Locate every blood parasite and identify its species.
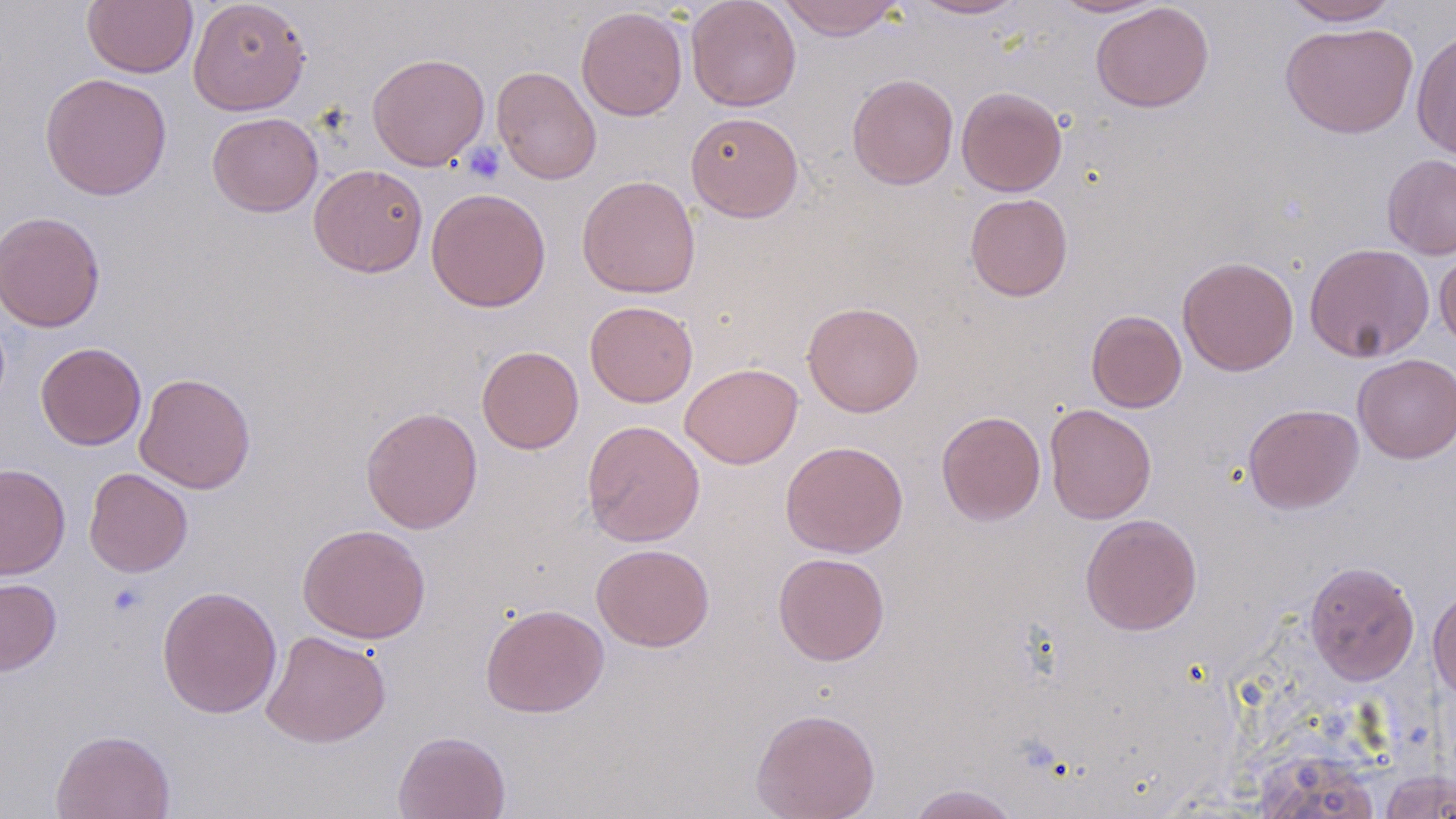
No blood parasites observed.

slide-level diagnosis = no evidence of blood parasites
uninfected red blood cell locations = approximate bounding boxes as [x1, y1, x2, y2] in pixels: [82, 0, 198, 78], [187, 0, 311, 115], [686, 0, 802, 111], [777, 0, 905, 40], [910, 0, 1027, 20], [1054, 0, 1164, 17], [1282, 0, 1400, 26], [1090, 2, 1214, 113], [576, 6, 688, 121], [1280, 21, 1418, 138], [1411, 28, 1456, 161], [367, 52, 489, 171], [491, 65, 601, 185], [40, 72, 173, 201], [847, 73, 959, 189], [956, 86, 1068, 196], [207, 111, 323, 217], [686, 111, 803, 222], [1382, 154, 1456, 259], [308, 163, 428, 277], [577, 175, 701, 298], [425, 187, 551, 312], [964, 193, 1073, 301], [0, 209, 105, 333], [1304, 242, 1434, 363], [1434, 250, 1456, 353], [1177, 256, 1299, 376], [585, 300, 698, 407], [802, 301, 924, 417], [1086, 309, 1187, 412], [35, 342, 146, 450], [476, 346, 584, 453], [1353, 354, 1456, 463], [680, 362, 803, 469], [134, 372, 256, 494], [1044, 403, 1157, 524], [1243, 403, 1364, 514], [361, 406, 483, 533], [936, 410, 1046, 525], [582, 420, 705, 546], [780, 441, 908, 558], [0, 462, 70, 580], [83, 467, 193, 577], [1079, 514, 1203, 635], [297, 523, 431, 644], [592, 543, 714, 652], [773, 552, 890, 665], [1303, 560, 1420, 685], [0, 577, 61, 677], [1428, 585, 1456, 703], [157, 586, 282, 719], [480, 603, 609, 718], [261, 630, 392, 748], [751, 707, 880, 819], [51, 729, 176, 819], [392, 730, 511, 819], [1254, 750, 1382, 819], [1379, 769, 1456, 818], [907, 783, 1022, 819]
platelet locations = approximate bounding boxes as [x1, y1, x2, y2] in pixels: [463, 142, 505, 184], [107, 583, 147, 617]
preparation = thin blood smear
image size = 1456×819 pixels
magnification = 1000x
modality = optical microscopy
stain = May-Grünwald-Giemsa
field of view = one of a larger specimen